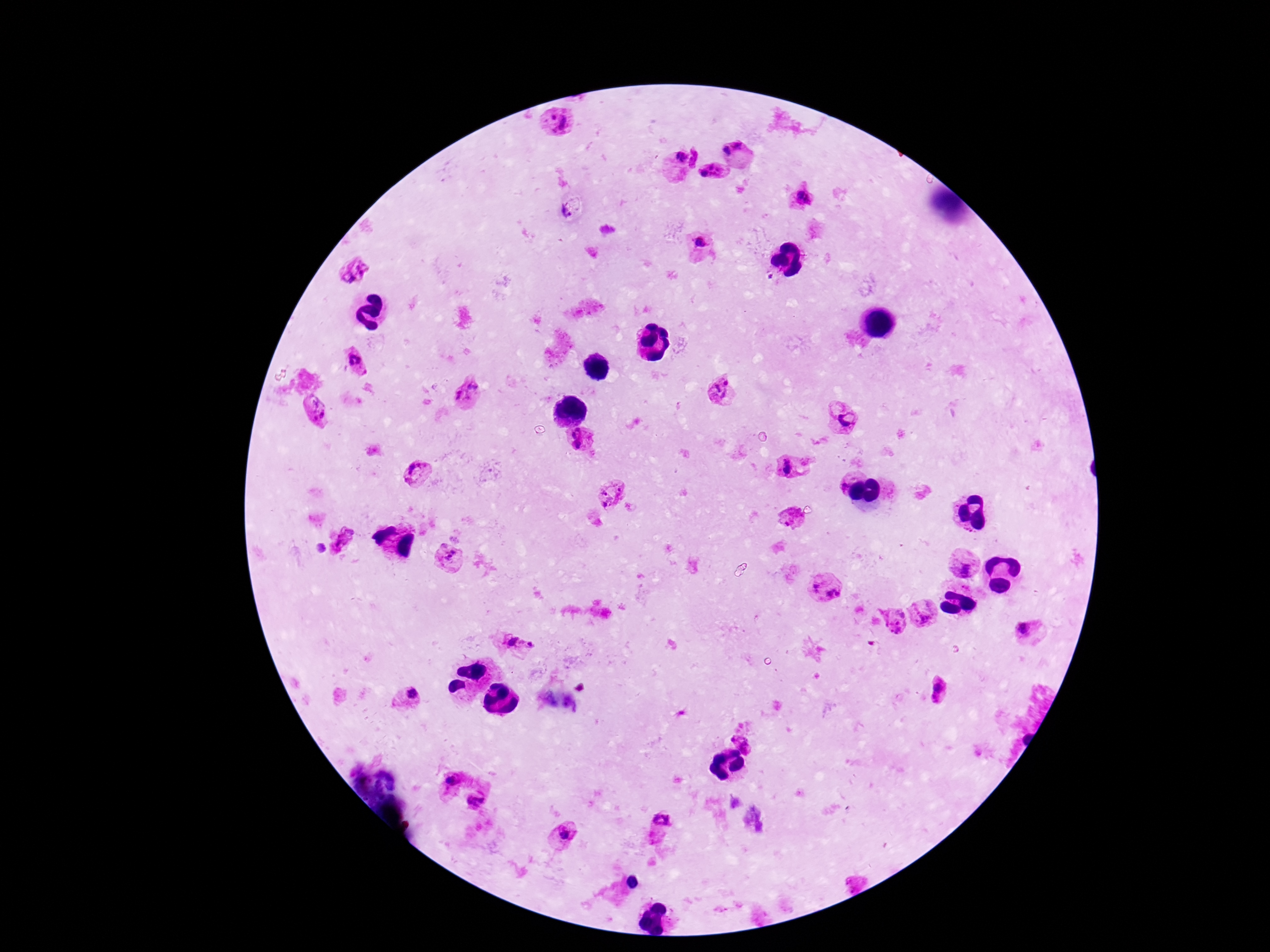

{
  "image_size": "1270×952 pixels",
  "preparation": "thick blood smear",
  "stain": "Giemsa",
  "field_of_view": "single",
  "patient_malaria_status": "positive",
  "capture": "smartphone camera through the microscope eyepiece",
  "magnification": "100x",
  "plasmodium_parasite_locations": "approximate centers as (x, y) in pixels: (739, 144), (727, 150), (680, 156), (711, 172), (803, 196), (565, 214), (701, 244), (354, 268), (356, 358), (721, 390), (468, 392), (314, 411), (846, 416), (581, 439), (789, 469), (416, 473), (844, 481), (611, 494), (791, 520), (342, 540), (322, 549), (451, 556), (965, 562), (816, 587), (833, 592), (925, 614), (895, 621), (1023, 628), (514, 641), (531, 644), (938, 688), (411, 694), (745, 738), (451, 780), (476, 799), (661, 822), (565, 832)"
}